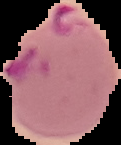
Summary:
  - Image type: cell region segmented out of the field of view; surrounding area masked to black
  - Image size: 121×145 pixels
  - Malaria status: parasitized
  - Preparation: thin blood smear